Give the extent of all Plasmodium ovale-infected red blood cells.
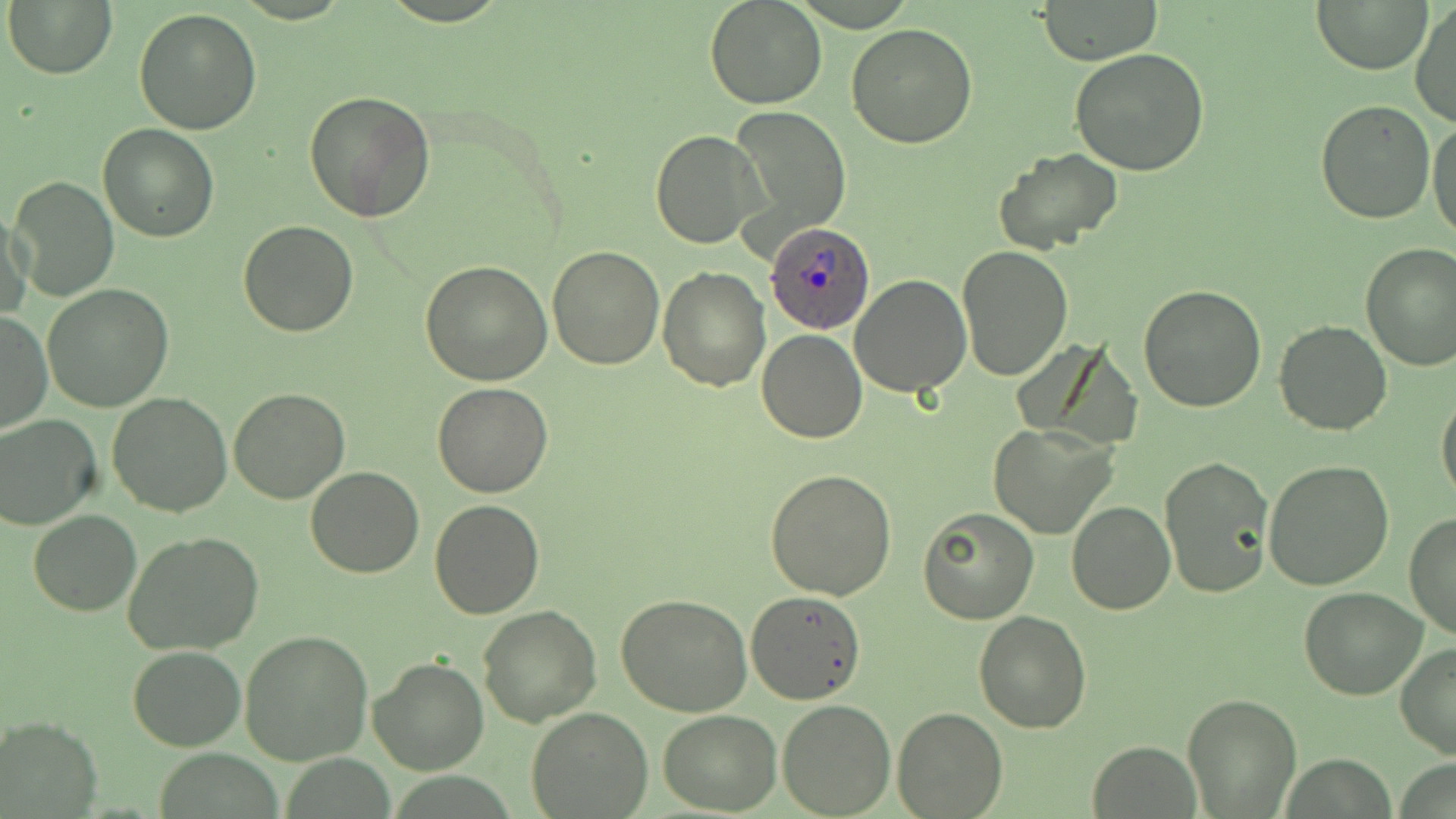
Approximate bounding boxes as named x1/y1/x2/y2 corners in pixels.
Plasmodium ovale-infected red blood cells: (x1=765, y1=224, x2=874, y2=337).

Uninfected red blood cell locations: (x1=704, y1=0, x2=827, y2=109), (x1=1039, y1=0, x2=1163, y2=66), (x1=6, y1=1, x2=117, y2=79), (x1=1314, y1=1, x2=1430, y2=74), (x1=1410, y1=2, x2=1456, y2=128), (x1=134, y1=9, x2=262, y2=135), (x1=846, y1=22, x2=979, y2=149), (x1=1070, y1=48, x2=1210, y2=176), (x1=303, y1=89, x2=437, y2=225), (x1=1314, y1=100, x2=1435, y2=223), (x1=728, y1=105, x2=851, y2=244), (x1=1427, y1=119, x2=1456, y2=240), (x1=99, y1=123, x2=218, y2=242), (x1=650, y1=130, x2=764, y2=249), (x1=995, y1=146, x2=1125, y2=256), (x1=9, y1=176, x2=119, y2=302), (x1=2, y1=208, x2=32, y2=324), (x1=238, y1=219, x2=358, y2=337), (x1=1359, y1=244, x2=1456, y2=371), (x1=547, y1=245, x2=666, y2=369), (x1=957, y1=245, x2=1074, y2=379), (x1=422, y1=261, x2=553, y2=385), (x1=658, y1=266, x2=771, y2=390), (x1=851, y1=273, x2=970, y2=395), (x1=1137, y1=284, x2=1267, y2=412), (x1=42, y1=285, x2=174, y2=412), (x1=1, y1=309, x2=51, y2=434), (x1=1273, y1=320, x2=1394, y2=435), (x1=757, y1=329, x2=867, y2=443), (x1=432, y1=382, x2=555, y2=498), (x1=228, y1=387, x2=351, y2=504), (x1=1436, y1=388, x2=1456, y2=508), (x1=108, y1=393, x2=232, y2=516), (x1=0, y1=414, x2=103, y2=530), (x1=988, y1=422, x2=1117, y2=539), (x1=1160, y1=453, x2=1273, y2=598), (x1=1263, y1=459, x2=1395, y2=592), (x1=766, y1=466, x2=898, y2=599), (x1=304, y1=467, x2=425, y2=578), (x1=429, y1=500, x2=546, y2=620), (x1=1067, y1=502, x2=1176, y2=616), (x1=917, y1=506, x2=1038, y2=624), (x1=29, y1=510, x2=140, y2=615), (x1=1404, y1=511, x2=1456, y2=642), (x1=123, y1=531, x2=264, y2=656), (x1=1299, y1=586, x2=1427, y2=699), (x1=745, y1=592, x2=866, y2=705), (x1=616, y1=596, x2=753, y2=716), (x1=476, y1=605, x2=602, y2=728), (x1=974, y1=609, x2=1090, y2=732), (x1=240, y1=629, x2=374, y2=765), (x1=1394, y1=641, x2=1456, y2=760), (x1=127, y1=645, x2=247, y2=749), (x1=368, y1=654, x2=489, y2=774), (x1=1182, y1=693, x2=1302, y2=817), (x1=777, y1=699, x2=895, y2=818), (x1=526, y1=706, x2=653, y2=819), (x1=894, y1=707, x2=1006, y2=817), (x1=658, y1=709, x2=781, y2=816), (x1=1, y1=715, x2=101, y2=817), (x1=1088, y1=740, x2=1201, y2=817). Slide-level diagnosis: Plasmodium ovale. 1000x magnification. Image is 1456×819 pixels. Light microscopy. Thin blood film. One field of a larger specimen. May-Grünwald-Giemsa stain.